Locate every uninfected red blood cell.
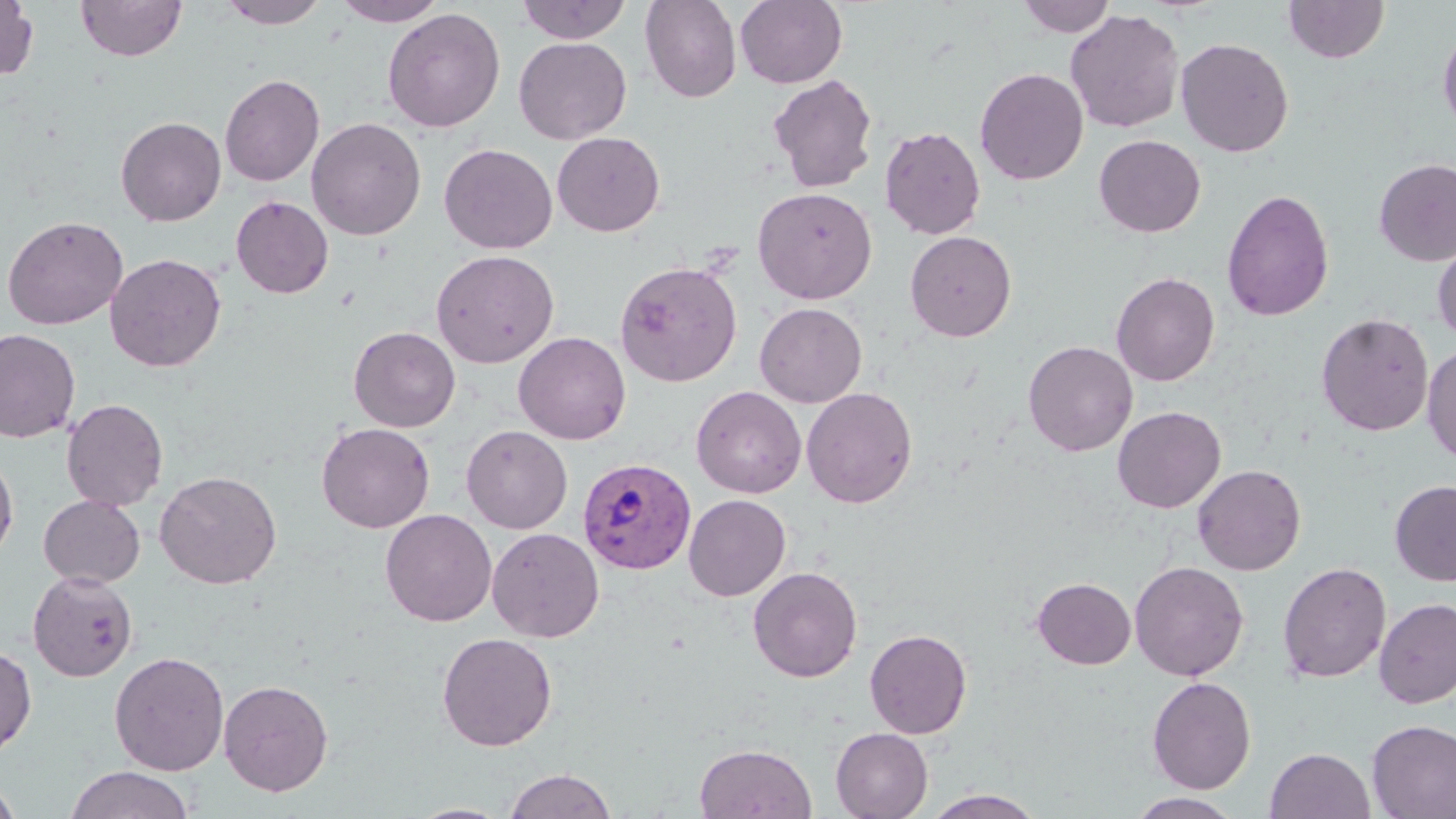
Approximate bounding boxes as (x1,y1)-(x2,y2) corner pairs in pixels.
Uninfected red blood cells: (77,0)-(186,61), (217,0)-(331,28), (332,0)-(449,26), (516,0)-(633,43), (640,0)-(742,103), (1016,0)-(1117,37), (1283,0)-(1389,63), (0,1)-(39,81), (736,1)-(847,88), (381,7)-(506,133), (1066,9)-(1184,133), (1438,23)-(1456,137), (514,37)-(632,144), (1176,37)-(1294,157), (974,68)-(1089,185), (220,73)-(325,187), (767,73)-(879,193), (115,116)-(226,226), (306,117)-(427,240), (879,125)-(986,240), (552,131)-(665,237), (1093,134)-(1206,237), (439,143)-(557,254), (1373,158)-(1456,266), (752,187)-(878,304), (1221,188)-(1335,322), (231,196)-(333,299), (2,215)-(128,329), (905,231)-(1017,342), (1432,234)-(1456,343), (430,249)-(559,369), (104,253)-(227,372), (614,260)-(742,387), (1111,271)-(1220,386), (754,302)-(867,407), (1316,312)-(1433,436), (349,326)-(460,432), (0,329)-(80,443), (514,332)-(631,444), (1023,340)-(1138,455), (1422,341)-(1456,464), (691,386)-(807,498), (801,387)-(918,508), (61,398)-(168,510), (1112,406)-(1226,512), (316,422)-(435,533), (461,425)-(573,534), (0,451)-(18,561), (1192,464)-(1306,576), (155,470)-(281,589), (1390,479)-(1456,586), (38,494)-(145,588), (683,494)-(791,601), (380,508)-(497,627), (486,527)-(604,642), (1129,561)-(1249,681), (1277,561)-(1392,683), (748,566)-(863,682), (28,570)-(138,682), (1032,577)-(1136,669), (1373,597)-(1456,708), (864,628)-(972,739), (436,632)-(557,751), (0,643)-(37,758), (109,651)-(230,776), (1146,676)-(1257,794), (218,679)-(334,796), (1367,720)-(1456,818), (830,728)-(933,819), (694,743)-(817,819), (1265,748)-(1375,819), (64,765)-(195,819), (504,768)-(618,818), (0,775)-(22,819), (922,789)-(1046,818), (1126,792)-(1242,818), (407,802)-(513,819).

Plasmodium vivax-infected red blood cell locations: (577,457)-(697,575). Slide-level diagnosis: Plasmodium vivax. May-Grünwald-Giemsa-stained preparation. Single field of view. Image is 1456×819 pixels. Light microscopy. 1000x magnification. Thin blood film.